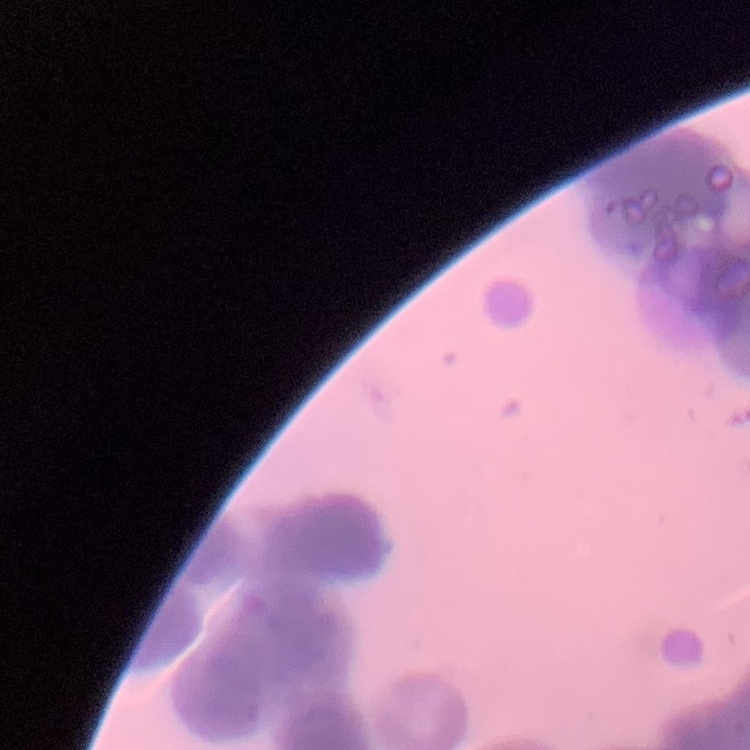 The erythrocytes show rouleaux formation. Thin blood film. Square crop of a larger photomicrograph. Stained with either Field's or Giemsa.